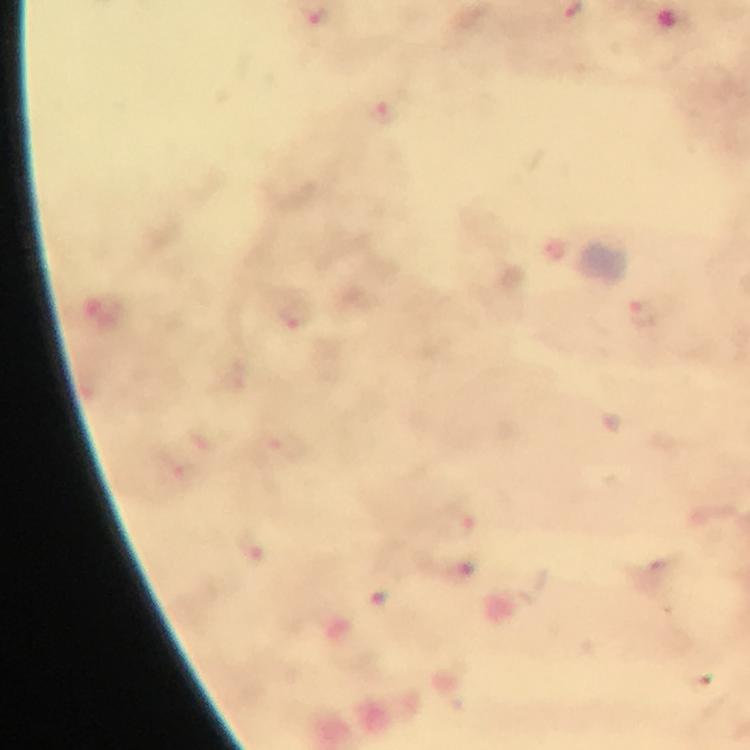
Approximate centers as (x, y) in pixels.
Summary:
  - Plasmodium parasite locations: (319, 21), (384, 110), (296, 320)
  - Context: from a malaria diagnostic workup
  - Magnification: 100x
  - Cropped from: a single field of view
  - Stain: Giemsa
  - Image size: 750×750 pixels
  - Preparation: thick blood smear
  - Immersion oil: used
  - Capture: smartphone mounted on the microscope